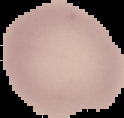

malaria status = uninfected
preparation = thin blood smear
image size = 124×118 pixels
image type = cell region segmented out of the field of view; surrounding area masked to black